Give the extent of all white blood cells.
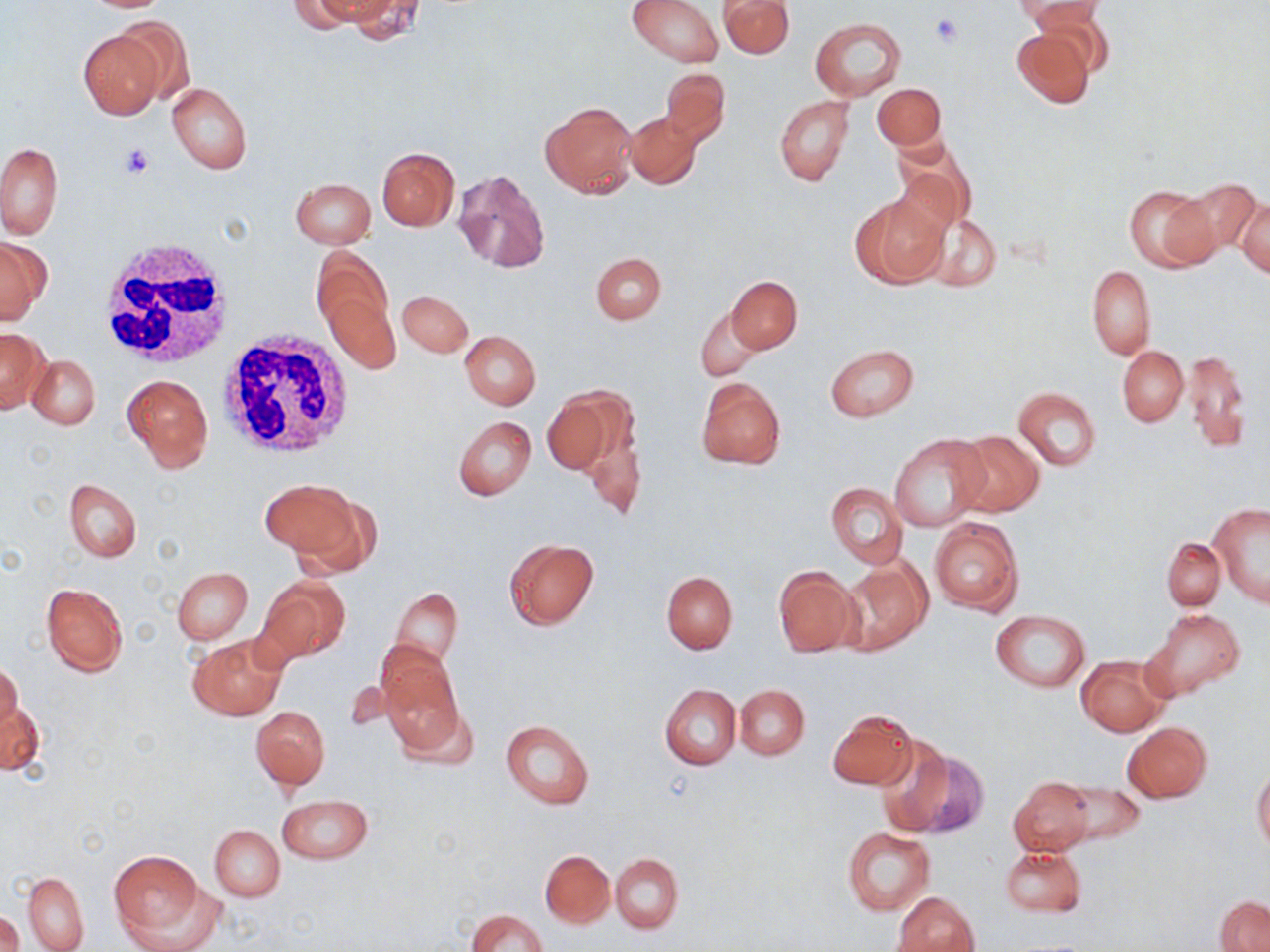

Approximate bounding boxes as named x1/y1/x2/y2 corners in pixels.
White blood cells: (x1=94, y1=238, x2=232, y2=372), (x1=216, y1=330, x2=356, y2=459).

slide-level diagnosis = no evidence of blood parasites
field of view = single
preparation = thin blood smear
stain = May-Grünwald-Giemsa
image size = 1270×952 pixels
uninfected red blood cell locations = approximate bounding boxes as named x1/y1/x2/y2 corners in pixels: (x1=288, y1=0, x2=375, y2=32), (x1=341, y1=0, x2=425, y2=43), (x1=628, y1=0, x2=724, y2=67), (x1=720, y1=0, x2=795, y2=57), (x1=1020, y1=0, x2=1105, y2=36), (x1=111, y1=17, x2=193, y2=108), (x1=811, y1=18, x2=904, y2=101), (x1=1010, y1=27, x2=1095, y2=108), (x1=78, y1=29, x2=168, y2=119), (x1=662, y1=67, x2=730, y2=146), (x1=167, y1=83, x2=252, y2=174), (x1=872, y1=83, x2=946, y2=150), (x1=775, y1=95, x2=854, y2=186), (x1=540, y1=100, x2=638, y2=198), (x1=624, y1=111, x2=702, y2=190), (x1=893, y1=140, x2=976, y2=234), (x1=1, y1=142, x2=62, y2=239), (x1=376, y1=148, x2=459, y2=230), (x1=451, y1=168, x2=550, y2=273), (x1=290, y1=178, x2=376, y2=249), (x1=1174, y1=178, x2=1261, y2=257), (x1=1123, y1=184, x2=1216, y2=271), (x1=850, y1=193, x2=948, y2=288), (x1=1236, y1=196, x2=1269, y2=279), (x1=923, y1=214, x2=1001, y2=292), (x1=0, y1=237, x2=50, y2=325), (x1=312, y1=249, x2=395, y2=346), (x1=591, y1=252, x2=666, y2=325), (x1=1086, y1=265, x2=1156, y2=359), (x1=726, y1=276, x2=802, y2=353), (x1=321, y1=286, x2=400, y2=374), (x1=398, y1=290, x2=471, y2=357), (x1=695, y1=307, x2=761, y2=382), (x1=0, y1=328, x2=48, y2=414), (x1=460, y1=331, x2=541, y2=410), (x1=825, y1=343, x2=919, y2=421), (x1=1118, y1=345, x2=1188, y2=426), (x1=1181, y1=350, x2=1250, y2=453), (x1=27, y1=354, x2=100, y2=430), (x1=123, y1=374, x2=213, y2=471), (x1=695, y1=377, x2=786, y2=468), (x1=1014, y1=387, x2=1101, y2=471), (x1=541, y1=390, x2=623, y2=475), (x1=577, y1=408, x2=646, y2=523), (x1=454, y1=416, x2=537, y2=501), (x1=950, y1=430, x2=1045, y2=518), (x1=890, y1=435, x2=990, y2=531), (x1=261, y1=475, x2=359, y2=561), (x1=64, y1=478, x2=141, y2=562), (x1=826, y1=483, x2=908, y2=569), (x1=286, y1=488, x2=383, y2=579), (x1=1208, y1=502, x2=1270, y2=607), (x1=929, y1=518, x2=1023, y2=615), (x1=503, y1=537, x2=599, y2=629), (x1=1162, y1=538, x2=1224, y2=610), (x1=837, y1=559, x2=931, y2=656), (x1=772, y1=566, x2=858, y2=656), (x1=171, y1=567, x2=252, y2=643), (x1=662, y1=572, x2=737, y2=654), (x1=258, y1=576, x2=350, y2=664), (x1=41, y1=582, x2=128, y2=677), (x1=389, y1=588, x2=463, y2=672), (x1=1143, y1=609, x2=1245, y2=702), (x1=990, y1=611, x2=1091, y2=692), (x1=188, y1=634, x2=286, y2=721), (x1=376, y1=645, x2=463, y2=749), (x1=1076, y1=655, x2=1170, y2=737), (x1=1, y1=661, x2=24, y2=737), (x1=661, y1=684, x2=741, y2=770), (x1=735, y1=684, x2=809, y2=760), (x1=1, y1=698, x2=46, y2=778), (x1=251, y1=706, x2=329, y2=790), (x1=827, y1=709, x2=917, y2=789), (x1=500, y1=719, x2=595, y2=809), (x1=1121, y1=721, x2=1214, y2=804), (x1=895, y1=745, x2=988, y2=838), (x1=1252, y1=768, x2=1270, y2=852), (x1=1008, y1=777, x2=1093, y2=856), (x1=1058, y1=780, x2=1145, y2=847), (x1=276, y1=795, x2=373, y2=863), (x1=210, y1=824, x2=285, y2=901), (x1=843, y1=826, x2=934, y2=914), (x1=999, y1=845, x2=1087, y2=919), (x1=109, y1=850, x2=205, y2=939), (x1=540, y1=850, x2=614, y2=927), (x1=610, y1=853, x2=682, y2=934), (x1=22, y1=872, x2=89, y2=952), (x1=894, y1=891, x2=979, y2=952), (x1=1215, y1=895, x2=1269, y2=952), (x1=467, y1=910, x2=547, y2=952), (x1=0, y1=911, x2=24, y2=952)
magnification = 1000x
modality = optical microscopy
platelet locations = approximate bounding boxes as named x1/y1/x2/y2 corners in pixels: (x1=931, y1=13, x2=963, y2=46), (x1=119, y1=142, x2=155, y2=179)